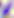 Photomicrograph. 400x magnification. Toxoplasma gondii is seen.